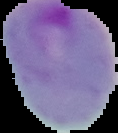
preparation = thin blood smear
result = malaria parasites identified
image size = 118×133 pixels
image type = cell region segmented out of the field of view; surrounding area masked to black